Identify the blood parasite species.
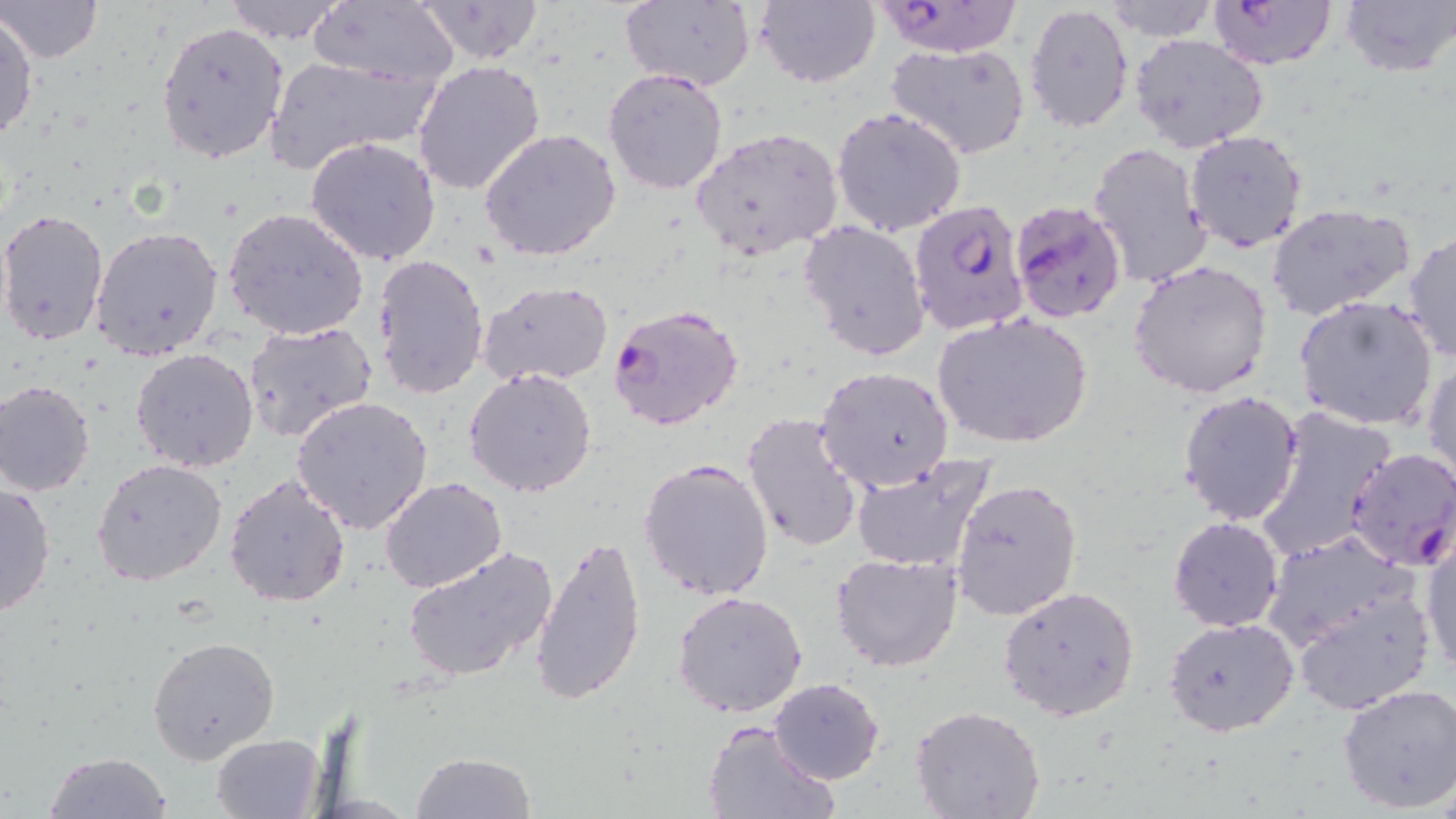
Plasmodium falciparum.

field of view = one of a larger specimen
magnification = 1000x
uninfected red blood cell locations = approximate bounding boxes as (x1, y1, x2, y2) in pixels: (1, 0, 102, 63), (410, 0, 548, 65), (617, 0, 756, 93), (753, 0, 880, 88), (1105, 0, 1217, 41), (1340, 0, 1454, 76), (223, 1, 348, 44), (307, 1, 458, 88), (1023, 3, 1133, 133), (0, 13, 39, 147), (156, 20, 289, 164), (1129, 35, 1270, 155), (884, 42, 1031, 162), (263, 53, 439, 173), (413, 59, 548, 197), (602, 68, 729, 194), (831, 107, 966, 237), (479, 127, 624, 263), (692, 127, 844, 259), (1182, 129, 1308, 253), (305, 137, 441, 266), (1087, 141, 1211, 287), (1266, 202, 1414, 321), (0, 207, 111, 346), (222, 207, 370, 342), (800, 220, 930, 362), (90, 226, 224, 362), (1403, 229, 1456, 366), (371, 252, 490, 400), (1130, 260, 1274, 400), (478, 281, 614, 387), (1294, 295, 1439, 430), (931, 310, 1095, 452), (242, 321, 378, 445), (129, 348, 259, 473), (1423, 360, 1456, 491), (813, 366, 954, 494), (465, 367, 598, 499), (1, 380, 97, 497), (1177, 390, 1305, 527), (291, 395, 435, 535), (1255, 406, 1397, 564), (741, 412, 864, 553), (848, 452, 998, 574), (637, 457, 776, 602), (92, 458, 228, 587), (223, 474, 352, 609), (379, 477, 508, 591), (949, 478, 1081, 623), (0, 482, 56, 619), (1167, 516, 1285, 632), (1420, 526, 1456, 678), (1261, 530, 1418, 656), (532, 533, 650, 709), (402, 546, 558, 683), (830, 552, 964, 674), (1289, 581, 1437, 715), (999, 585, 1140, 721), (673, 591, 808, 717), (1163, 616, 1299, 737), (148, 633, 280, 765), (770, 677, 884, 785), (1335, 684, 1456, 813), (910, 706, 1046, 818), (701, 720, 837, 818), (211, 733, 326, 819), (42, 752, 172, 819), (412, 752, 534, 819)
preparation = thin blood smear
modality = optical microscopy
Plasmodium falciparum-infected red blood cell locations = approximate bounding boxes as (x1, y1, x2, y2) in pixels: (1205, 0, 1336, 71), (873, 2, 1024, 58), (1007, 198, 1129, 325), (909, 201, 1030, 338), (606, 304, 746, 431), (1345, 448, 1456, 572)
image size = 1456×819 pixels
stain = May-Grünwald-Giemsa